Report the malaria status of this cell.
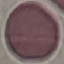

It is uninfected.

Summary:
  - Stain: Giemsa
  - Capture: smartphone through the microscope eyepiece
  - Preparation: thin blood smear
  - Image type: automatically extracted cell patch, resized to 64 × 64 pixels